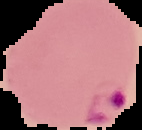
Summary:
  - Preparation: thin blood smear
  - Image type: segmented cell region on a black background
  - Image size: 142×130 pixels
  - Result: malaria parasites detected